Evaluate for malaria.
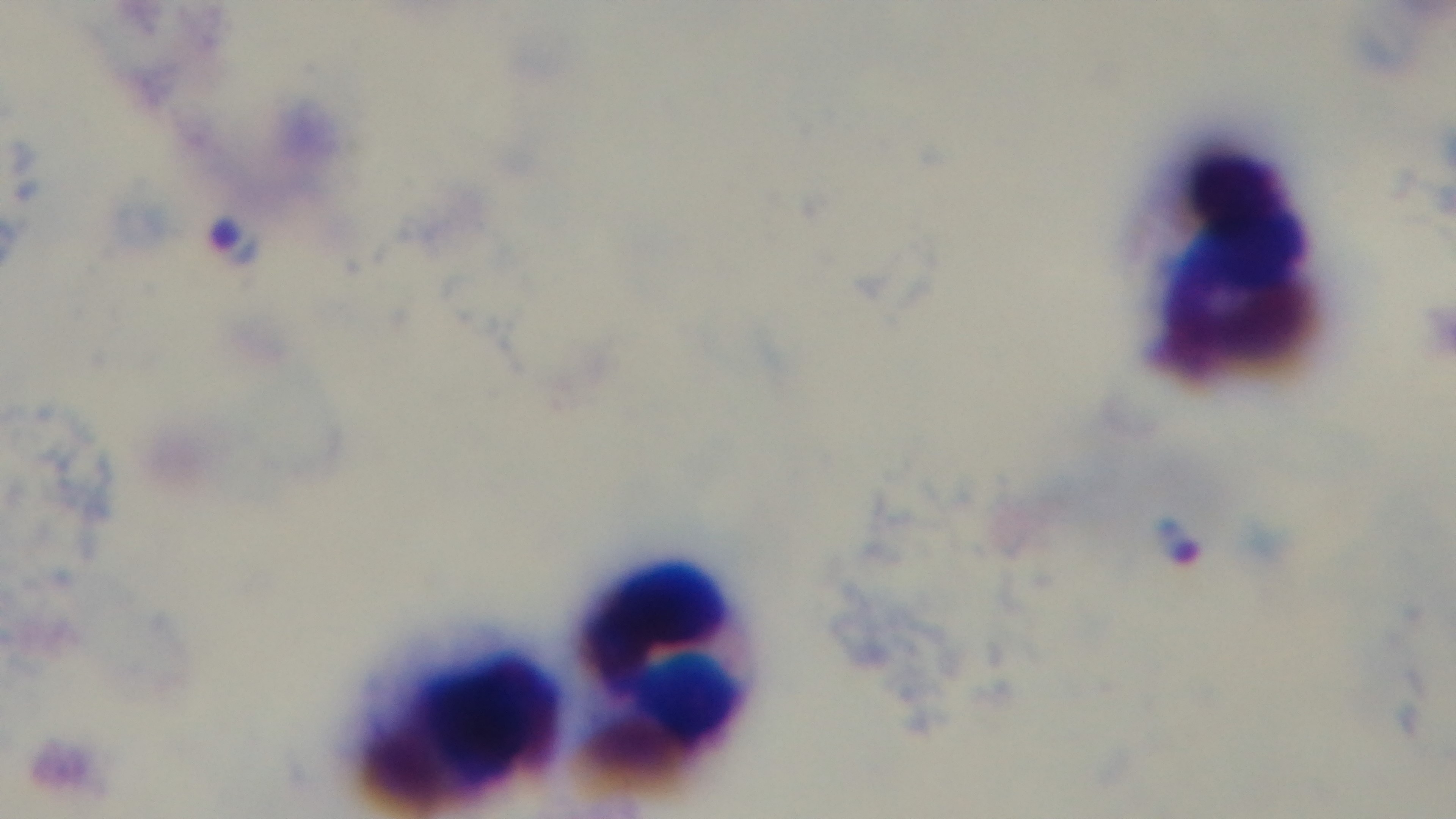
Infected.

100x oil-immersion objective. Captured with a mounted 4K digital camera. Preparation: thick. Photomicrograph. Giemsa-stained. One field from the slide.